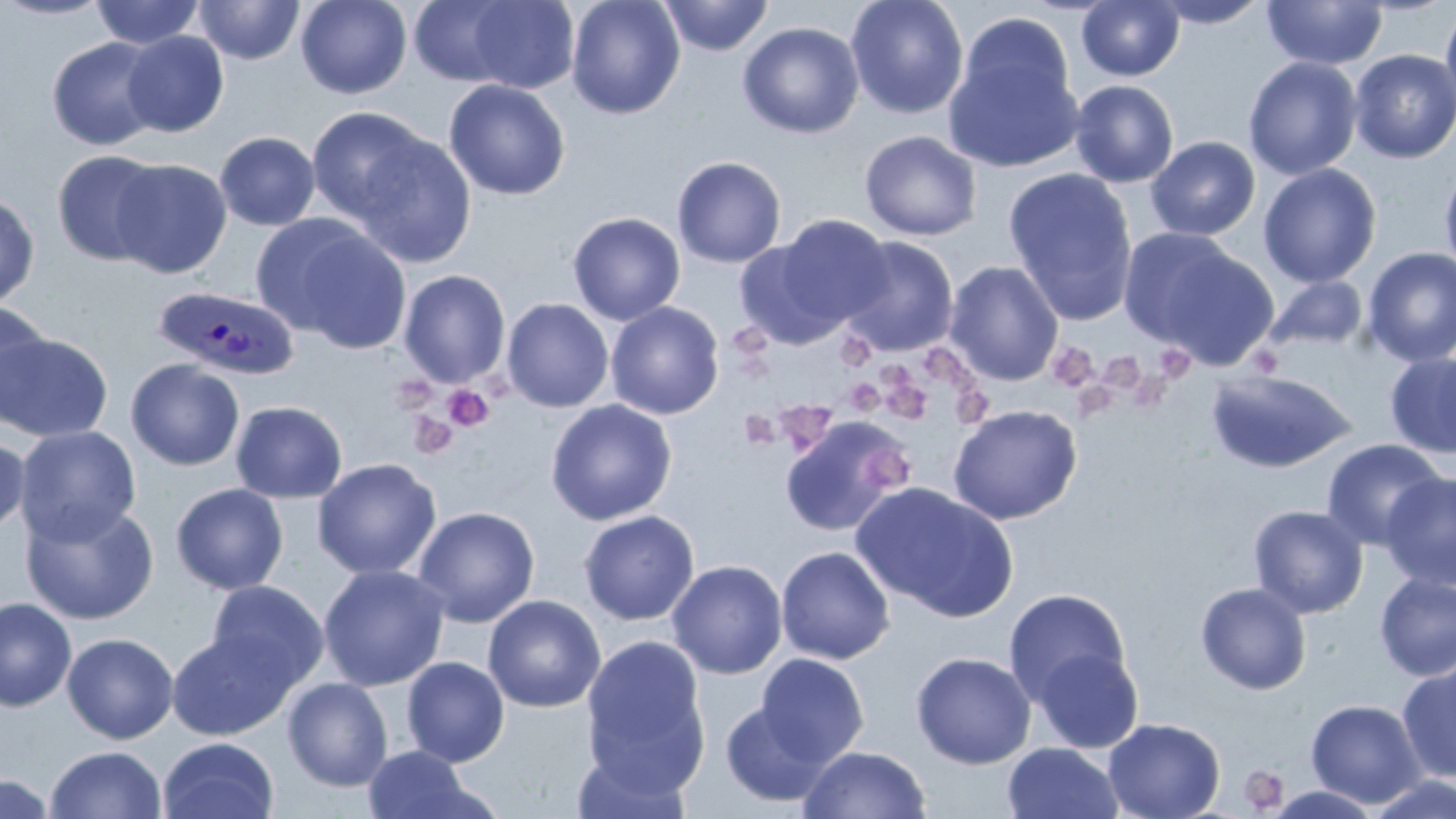
Summary:
  - Coordinate format: approximate bounding boxes as (x1, y1, x2, y2) in pixels
  - Platelet locations: (727, 326, 772, 357), (835, 332, 874, 367), (1050, 346, 1099, 391), (926, 348, 979, 390), (1156, 349, 1199, 380), (1098, 353, 1145, 393), (877, 370, 932, 425), (1133, 372, 1172, 414), (844, 377, 885, 416), (394, 381, 437, 418), (442, 385, 494, 433), (956, 387, 991, 423), (1075, 387, 1118, 422), (782, 405, 835, 450), (738, 410, 779, 450), (407, 411, 458, 460), (865, 447, 914, 490), (1238, 765, 1290, 814)
  - Uninfected red blood cell locations: (0, 0, 114, 21), (90, 0, 205, 49), (194, 0, 305, 64), (296, 0, 411, 99), (566, 0, 685, 119), (658, 0, 775, 56), (845, 0, 969, 119), (1148, 0, 1271, 28), (409, 1, 528, 87), (1076, 1, 1185, 81), (1262, 1, 1388, 70), (460, 2, 581, 93), (1440, 3, 1456, 122), (944, 18, 1081, 172), (737, 21, 864, 139), (120, 31, 229, 137), (46, 36, 165, 151), (1349, 49, 1456, 163), (1243, 57, 1362, 180), (443, 79, 571, 201), (1069, 80, 1179, 187), (306, 107, 431, 224), (859, 130, 983, 241), (215, 132, 320, 231), (853, 132, 974, 359), (353, 134, 476, 267), (1146, 136, 1261, 240), (51, 150, 168, 266), (672, 155, 787, 268), (110, 159, 232, 279), (1440, 162, 1456, 281), (1259, 164, 1381, 288), (1002, 167, 1139, 325), (0, 192, 40, 310), (567, 211, 686, 325), (769, 215, 893, 332), (289, 224, 413, 354), (1121, 228, 1277, 369), (295, 235, 508, 379), (839, 236, 959, 357), (734, 238, 853, 349), (1361, 247, 1456, 367), (944, 261, 1064, 386), (398, 269, 511, 388), (1265, 276, 1368, 352), (501, 298, 614, 412), (0, 299, 50, 423), (605, 301, 725, 419), (1, 333, 113, 442), (1385, 352, 1456, 459), (125, 358, 245, 471), (1204, 369, 1357, 474), (546, 399, 677, 526), (230, 401, 347, 503), (947, 404, 1083, 525), (778, 415, 909, 537), (15, 425, 142, 546), (0, 435, 30, 537), (1321, 438, 1447, 550), (312, 459, 442, 580), (1380, 472, 1456, 592), (851, 482, 1019, 623), (170, 483, 289, 595), (20, 501, 159, 625), (1248, 505, 1369, 619), (411, 506, 539, 627), (579, 510, 700, 625), (776, 546, 895, 664), (667, 560, 787, 679), (319, 565, 449, 691), (1374, 573, 1456, 681), (206, 580, 328, 690), (1194, 582, 1311, 694), (1003, 588, 1132, 709), (483, 594, 605, 713), (0, 597, 76, 712), (167, 628, 298, 740), (62, 632, 179, 744), (580, 634, 710, 792), (1031, 646, 1143, 753), (911, 651, 1036, 769), (755, 654, 869, 765), (401, 656, 510, 767), (1397, 663, 1456, 785), (282, 676, 394, 792), (1305, 699, 1426, 808), (720, 700, 833, 807), (1103, 718, 1226, 819), (158, 736, 279, 819), (1002, 742, 1124, 819), (44, 745, 167, 819), (360, 745, 489, 819), (570, 745, 693, 819), (798, 745, 932, 819), (0, 773, 58, 819), (1365, 773, 1456, 818), (1263, 785, 1383, 818)
  - Plasmodium ovale-infected red blood cell locations: (153, 285, 300, 381)
  - Slide-level diagnosis: Plasmodium ovale
  - Field of view: single
  - Modality: optical microscopy
  - Preparation: thin blood smear
  - Stain: May-Grünwald-Giemsa
  - Magnification: 1000x
  - Image size: 1456×819 pixels